Locate every blood parasite and identify its species.
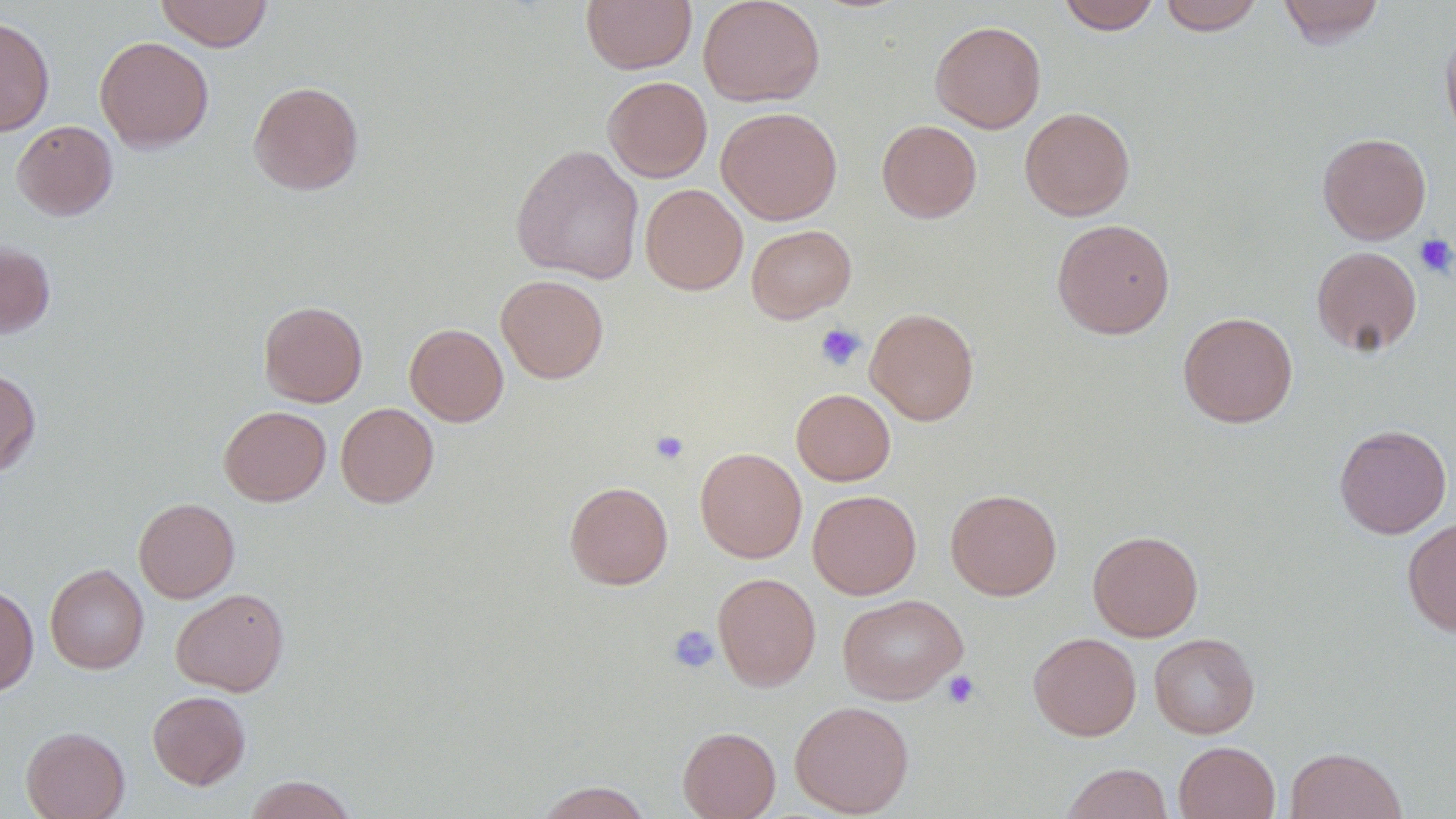

No blood parasites observed.

Approximate bounding boxes as named x1/y1/x2/y2 corners in pixels. Platelet locations: (x1=1413, y1=233, x2=1456, y2=278), (x1=814, y1=322, x2=866, y2=371), (x1=650, y1=430, x2=689, y2=464), (x1=667, y1=624, x2=720, y2=674), (x1=943, y1=670, x2=980, y2=709). Uninfected red blood cell locations: (x1=155, y1=0, x2=272, y2=51), (x1=581, y1=0, x2=697, y2=74), (x1=698, y1=0, x2=825, y2=107), (x1=1056, y1=0, x2=1162, y2=35), (x1=1158, y1=0, x2=1265, y2=35), (x1=1276, y1=0, x2=1386, y2=47), (x1=0, y1=14, x2=55, y2=136), (x1=930, y1=20, x2=1046, y2=133), (x1=1440, y1=22, x2=1456, y2=146), (x1=94, y1=35, x2=214, y2=153), (x1=602, y1=76, x2=712, y2=182), (x1=248, y1=80, x2=364, y2=196), (x1=716, y1=106, x2=842, y2=224), (x1=1019, y1=106, x2=1135, y2=221), (x1=11, y1=120, x2=118, y2=220), (x1=877, y1=120, x2=982, y2=222), (x1=1317, y1=132, x2=1431, y2=244), (x1=510, y1=144, x2=645, y2=284), (x1=640, y1=183, x2=748, y2=295), (x1=1051, y1=219, x2=1175, y2=339), (x1=745, y1=224, x2=856, y2=323), (x1=0, y1=241, x2=56, y2=339), (x1=1311, y1=245, x2=1422, y2=356), (x1=496, y1=274, x2=609, y2=383), (x1=258, y1=300, x2=368, y2=407), (x1=865, y1=307, x2=979, y2=425), (x1=1178, y1=311, x2=1298, y2=427), (x1=405, y1=323, x2=508, y2=426), (x1=0, y1=368, x2=41, y2=476), (x1=791, y1=388, x2=895, y2=486), (x1=336, y1=402, x2=439, y2=508), (x1=218, y1=405, x2=331, y2=506), (x1=1334, y1=424, x2=1452, y2=539), (x1=695, y1=447, x2=806, y2=562), (x1=564, y1=481, x2=673, y2=589), (x1=945, y1=488, x2=1062, y2=600), (x1=808, y1=490, x2=921, y2=599), (x1=134, y1=497, x2=240, y2=603), (x1=1402, y1=517, x2=1456, y2=636), (x1=1088, y1=530, x2=1203, y2=641), (x1=45, y1=563, x2=148, y2=674), (x1=712, y1=572, x2=821, y2=690), (x1=0, y1=584, x2=39, y2=696), (x1=171, y1=588, x2=290, y2=696), (x1=837, y1=594, x2=968, y2=704), (x1=1028, y1=632, x2=1141, y2=741), (x1=1149, y1=633, x2=1260, y2=738), (x1=147, y1=691, x2=251, y2=790), (x1=789, y1=700, x2=914, y2=817), (x1=20, y1=726, x2=130, y2=819), (x1=677, y1=726, x2=780, y2=819), (x1=1174, y1=741, x2=1280, y2=819), (x1=1285, y1=747, x2=1407, y2=818), (x1=1060, y1=762, x2=1174, y2=819), (x1=243, y1=775, x2=359, y2=819), (x1=533, y1=781, x2=653, y2=819). Slide-level diagnosis: negative for blood parasites. Thin blood smear. Single field of view. 1000x magnification. Image is 1456×819 pixels. Light microscopy.